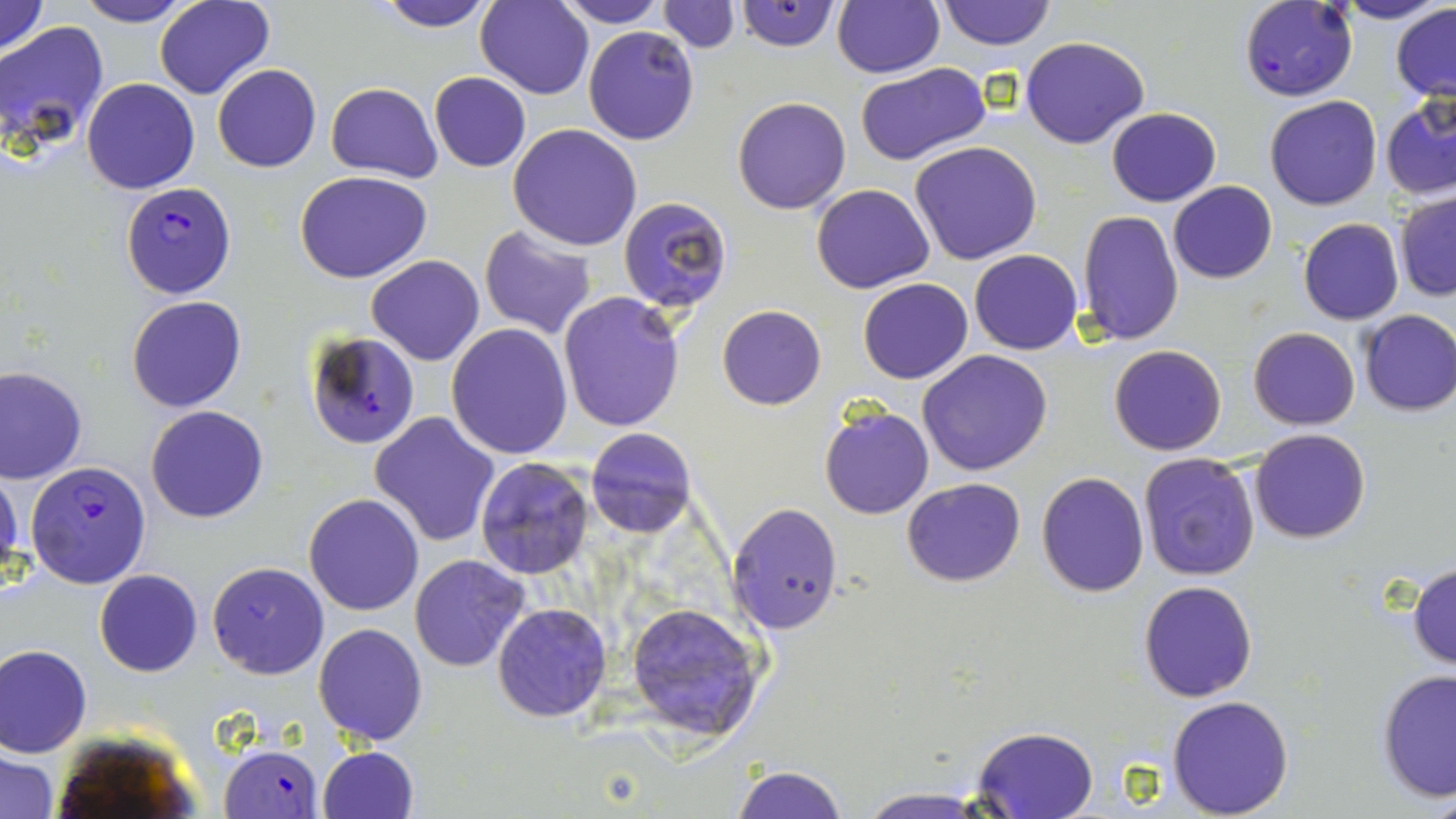
Summary:
  - Coordinate format: approximate bounding boxes as named x1/y1/x2/y2 corners in pixels
  - Uninfected red blood cell locations: (x1=75, y1=0, x2=195, y2=27), (x1=154, y1=0, x2=274, y2=100), (x1=377, y1=0, x2=496, y2=31), (x1=476, y1=0, x2=594, y2=99), (x1=552, y1=0, x2=669, y2=27), (x1=733, y1=0, x2=840, y2=51), (x1=936, y1=0, x2=1055, y2=51), (x1=1333, y1=0, x2=1453, y2=25), (x1=0, y1=1, x2=49, y2=58), (x1=658, y1=1, x2=738, y2=52), (x1=831, y1=1, x2=943, y2=78), (x1=840, y1=2, x2=959, y2=157), (x1=1391, y1=4, x2=1456, y2=103), (x1=1, y1=21, x2=109, y2=148), (x1=583, y1=26, x2=699, y2=146), (x1=1020, y1=36, x2=1149, y2=150), (x1=855, y1=62, x2=990, y2=166), (x1=212, y1=63, x2=321, y2=173), (x1=428, y1=72, x2=531, y2=172), (x1=82, y1=77, x2=200, y2=194), (x1=326, y1=82, x2=441, y2=182), (x1=1381, y1=93, x2=1456, y2=202), (x1=1264, y1=95, x2=1382, y2=210), (x1=733, y1=96, x2=852, y2=215), (x1=1107, y1=108, x2=1221, y2=206), (x1=508, y1=124, x2=642, y2=250), (x1=909, y1=142, x2=1043, y2=265), (x1=294, y1=171, x2=433, y2=282), (x1=1169, y1=181, x2=1277, y2=284), (x1=810, y1=184, x2=935, y2=294), (x1=1394, y1=192, x2=1456, y2=302), (x1=619, y1=197, x2=730, y2=315), (x1=1075, y1=209, x2=1184, y2=346), (x1=1298, y1=218, x2=1403, y2=324), (x1=479, y1=225, x2=598, y2=339), (x1=969, y1=249, x2=1083, y2=354), (x1=367, y1=255, x2=484, y2=366), (x1=857, y1=266, x2=1083, y2=366), (x1=858, y1=278, x2=973, y2=384), (x1=558, y1=292, x2=687, y2=433), (x1=126, y1=295, x2=246, y2=413), (x1=718, y1=305, x2=825, y2=409), (x1=1358, y1=309, x2=1456, y2=415), (x1=446, y1=323, x2=574, y2=459), (x1=1248, y1=326, x2=1360, y2=430), (x1=302, y1=330, x2=423, y2=451), (x1=1109, y1=345, x2=1226, y2=456), (x1=918, y1=349, x2=1054, y2=476), (x1=0, y1=366, x2=87, y2=485), (x1=818, y1=404, x2=933, y2=519), (x1=146, y1=406, x2=269, y2=523), (x1=369, y1=409, x2=501, y2=547), (x1=585, y1=427, x2=695, y2=538), (x1=1249, y1=428, x2=1371, y2=543), (x1=1137, y1=452, x2=1261, y2=581), (x1=474, y1=456, x2=596, y2=578), (x1=1, y1=469, x2=25, y2=594), (x1=1035, y1=471, x2=1150, y2=597), (x1=901, y1=477, x2=1026, y2=587), (x1=303, y1=492, x2=422, y2=616), (x1=727, y1=502, x2=842, y2=635), (x1=409, y1=554, x2=532, y2=672), (x1=1408, y1=561, x2=1456, y2=671), (x1=207, y1=562, x2=327, y2=679), (x1=95, y1=570, x2=202, y2=676), (x1=1138, y1=580, x2=1257, y2=702), (x1=623, y1=600, x2=768, y2=742), (x1=493, y1=603, x2=612, y2=721), (x1=313, y1=623, x2=428, y2=747), (x1=1, y1=644, x2=92, y2=756), (x1=1377, y1=669, x2=1456, y2=804), (x1=1167, y1=695, x2=1295, y2=816), (x1=970, y1=726, x2=1099, y2=817), (x1=317, y1=746, x2=420, y2=819), (x1=2, y1=751, x2=61, y2=819), (x1=730, y1=765, x2=849, y2=819), (x1=854, y1=787, x2=996, y2=818)
  - Plasmodium falciparum-infected red blood cell locations: (x1=1238, y1=1, x2=1358, y2=103), (x1=121, y1=183, x2=237, y2=298), (x1=23, y1=461, x2=154, y2=590), (x1=221, y1=742, x2=321, y2=818)
  - Slide-level diagnosis: Plasmodium falciparum
  - Modality: optical microscopy
  - Image size: 1456×819 pixels
  - Magnification: 1000x
  - Stain: May-Grünwald-Giemsa
  - Field of view: one of a larger specimen
  - Preparation: thin blood smear